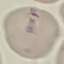

Summary:
  - Result: no malaria parasites detected
  - Stain: Giemsa
  - Capture: smartphone camera at the microscope eyepiece
  - Image type: cell patch, automatically extracted from a larger field of view and resized to 64 × 64 pixels
  - Preparation: thin blood smear